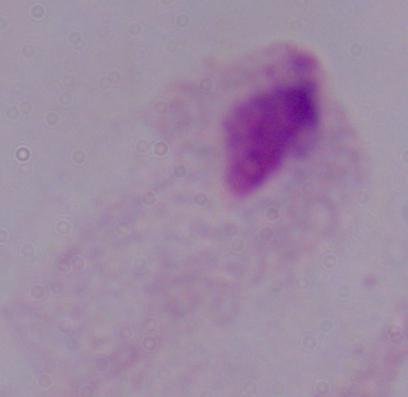
Summary:
  - Identification: trichomonad
  - Modality: micrograph
  - Magnification: 1000x